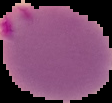

{
  "preparation": "thin blood film",
  "malaria_status": "parasitized",
  "image_type": "segmented cell region with the area outside set to black",
  "image_size": "112×103 pixels"
}